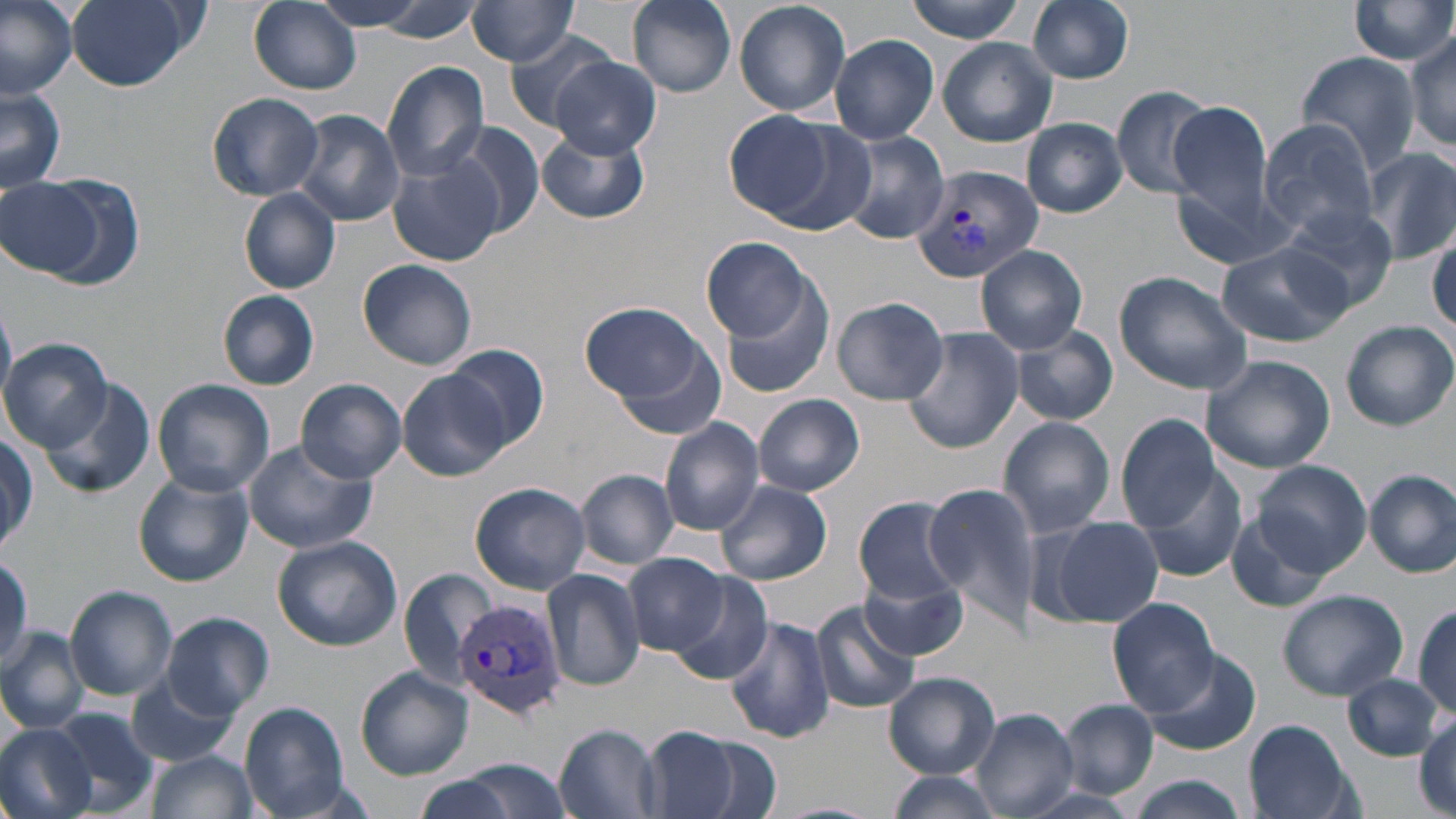
slide-level diagnosis = Plasmodium vivax
image size = 1456×819 pixels
magnification = 1000x
stain = May-Grünwald-Giemsa
field of view = one of a larger specimen
Plasmodium vivax-infected red blood cell locations = approximate bounding boxes as named x1/y1/x2/y2 corners in pixels: (x1=909, y1=162, x2=1044, y2=283), (x1=453, y1=594, x2=568, y2=720)
preparation = thin blood smear
uninfected red blood cell locations = approximate bounding boxes as named x1/y1/x2/y2 corners in pixels: (x1=0, y1=0, x2=77, y2=98), (x1=64, y1=0, x2=200, y2=91), (x1=248, y1=0, x2=362, y2=94), (x1=312, y1=0, x2=429, y2=31), (x1=355, y1=0, x2=487, y2=41), (x1=628, y1=0, x2=736, y2=96), (x1=734, y1=0, x2=853, y2=116), (x1=902, y1=0, x2=1029, y2=42), (x1=1349, y1=0, x2=1456, y2=68), (x1=464, y1=1, x2=582, y2=65), (x1=1027, y1=1, x2=1135, y2=84), (x1=1404, y1=30, x2=1456, y2=151), (x1=505, y1=32, x2=620, y2=131), (x1=829, y1=34, x2=939, y2=144), (x1=937, y1=38, x2=1058, y2=147), (x1=1294, y1=52, x2=1422, y2=178), (x1=551, y1=55, x2=662, y2=160), (x1=381, y1=61, x2=491, y2=181), (x1=0, y1=86, x2=67, y2=195), (x1=1111, y1=86, x2=1215, y2=200), (x1=207, y1=92, x2=324, y2=200), (x1=1167, y1=100, x2=1278, y2=237), (x1=294, y1=109, x2=405, y2=226), (x1=722, y1=110, x2=846, y2=224), (x1=1023, y1=118, x2=1126, y2=217), (x1=1258, y1=119, x2=1382, y2=241), (x1=448, y1=123, x2=544, y2=236), (x1=536, y1=127, x2=655, y2=225), (x1=840, y1=129, x2=951, y2=246), (x1=1360, y1=146, x2=1456, y2=265), (x1=388, y1=150, x2=504, y2=268), (x1=0, y1=173, x2=126, y2=285), (x1=239, y1=189, x2=341, y2=293), (x1=1280, y1=205, x2=1398, y2=311), (x1=1427, y1=231, x2=1456, y2=332), (x1=701, y1=236, x2=817, y2=342), (x1=1216, y1=241, x2=1352, y2=348), (x1=977, y1=246, x2=1088, y2=353), (x1=358, y1=257, x2=477, y2=370), (x1=1112, y1=270, x2=1254, y2=394), (x1=717, y1=271, x2=835, y2=401), (x1=218, y1=290, x2=319, y2=390), (x1=831, y1=295, x2=949, y2=405), (x1=580, y1=303, x2=714, y2=407), (x1=1340, y1=321, x2=1455, y2=430), (x1=1010, y1=325, x2=1118, y2=426), (x1=903, y1=327, x2=1023, y2=453), (x1=608, y1=331, x2=731, y2=440), (x1=3, y1=337, x2=112, y2=451), (x1=444, y1=343, x2=549, y2=452), (x1=1200, y1=353, x2=1336, y2=473), (x1=397, y1=370, x2=512, y2=482), (x1=152, y1=378, x2=273, y2=497), (x1=296, y1=378, x2=407, y2=483), (x1=41, y1=382, x2=155, y2=499), (x1=752, y1=394, x2=865, y2=497), (x1=1115, y1=414, x2=1222, y2=528), (x1=997, y1=416, x2=1115, y2=537), (x1=660, y1=417, x2=765, y2=536), (x1=1, y1=433, x2=39, y2=554), (x1=242, y1=440, x2=377, y2=555), (x1=1250, y1=460, x2=1372, y2=577), (x1=1133, y1=463, x2=1249, y2=585), (x1=576, y1=469, x2=678, y2=568), (x1=1365, y1=469, x2=1456, y2=579), (x1=132, y1=472, x2=253, y2=586), (x1=470, y1=481, x2=591, y2=594), (x1=716, y1=481, x2=833, y2=585), (x1=925, y1=485, x2=1038, y2=620), (x1=854, y1=495, x2=966, y2=612), (x1=1225, y1=509, x2=1335, y2=614), (x1=1046, y1=515, x2=1165, y2=629), (x1=272, y1=535, x2=403, y2=650), (x1=623, y1=553, x2=728, y2=655), (x1=0, y1=558, x2=29, y2=671), (x1=857, y1=560, x2=970, y2=663), (x1=398, y1=566, x2=498, y2=692), (x1=542, y1=567, x2=645, y2=690), (x1=667, y1=571, x2=774, y2=684), (x1=68, y1=585, x2=177, y2=700), (x1=1276, y1=588, x2=1408, y2=700), (x1=1106, y1=597, x2=1218, y2=715), (x1=1410, y1=599, x2=1456, y2=719), (x1=812, y1=601, x2=919, y2=713), (x1=160, y1=613, x2=277, y2=719), (x1=726, y1=617, x2=836, y2=744), (x1=0, y1=628, x2=89, y2=731), (x1=1141, y1=644, x2=1263, y2=758), (x1=356, y1=667, x2=474, y2=779), (x1=127, y1=671, x2=240, y2=767), (x1=884, y1=671, x2=998, y2=779), (x1=1343, y1=674, x2=1445, y2=762), (x1=1059, y1=700, x2=1158, y2=799), (x1=240, y1=702, x2=350, y2=818), (x1=971, y1=707, x2=1079, y2=818), (x1=45, y1=708, x2=160, y2=818), (x1=1415, y1=711, x2=1454, y2=814), (x1=1243, y1=719, x2=1358, y2=818), (x1=0, y1=724, x2=96, y2=819), (x1=554, y1=725, x2=663, y2=819), (x1=641, y1=726, x2=744, y2=818), (x1=681, y1=736, x2=784, y2=819), (x1=146, y1=748, x2=258, y2=819), (x1=447, y1=759, x2=576, y2=818), (x1=886, y1=771, x2=1006, y2=819), (x1=412, y1=775, x2=517, y2=819), (x1=1122, y1=775, x2=1248, y2=819), (x1=1013, y1=788, x2=1144, y2=819)
modality = optical microscopy